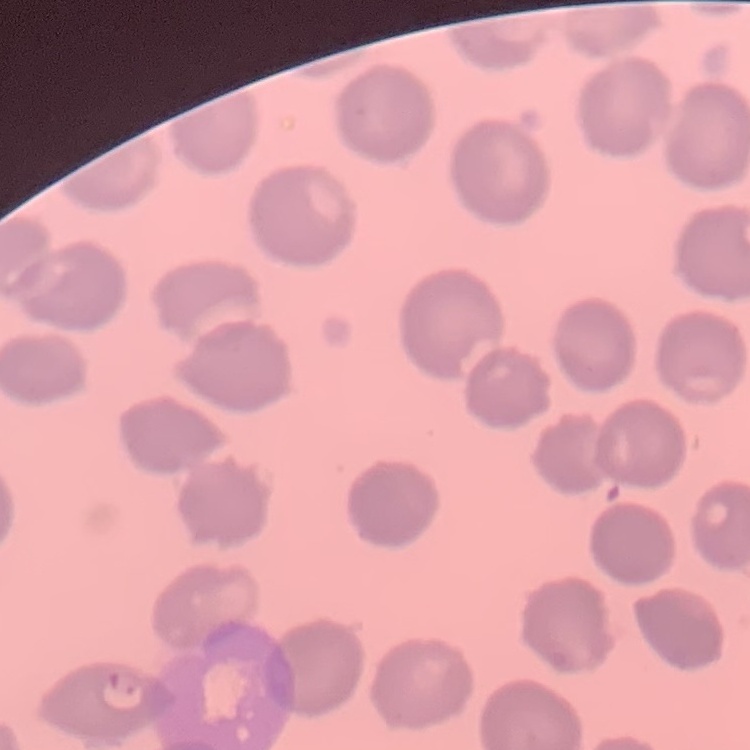

erythrocyte_morphology: no rouleaux formation
image_type: square crop of a larger photomicrograph
stain: Field's or Giemsa
preparation: thin blood film